Assess for malaria.
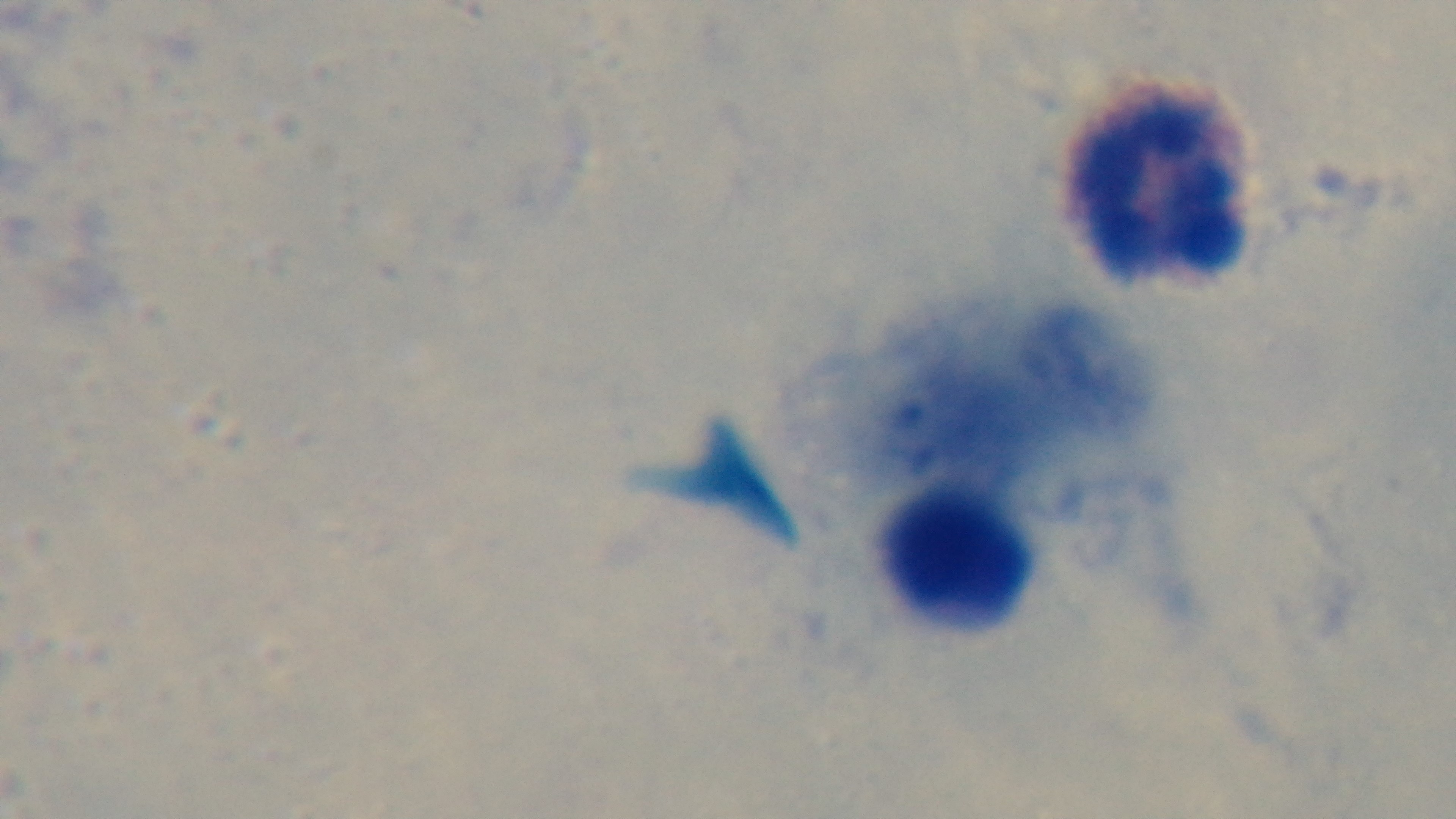

It is uninfected.

Preparation: thick blood film. Photomicrograph. 100x oil-immersion objective. One field from the slide. Mounted 4K digital camera. Giemsa-stained.